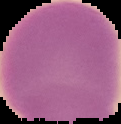

Summary:
  - Image size: 121×124 pixels
  - Preparation: thin blood film
  - Malaria status: uninfected
  - Image type: cell region segmented out of the field of view; surrounding area masked to black